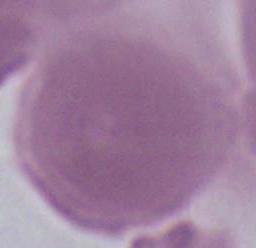

Captured at 1000x magnification. An erythrocyte is seen. Photomicrograph.